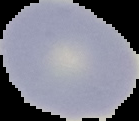
Image is 139×121 pixels. From a thin blood film. The area outside the segmented cell region is set to black. Result: no malaria parasites detected.